Classify the preparation.
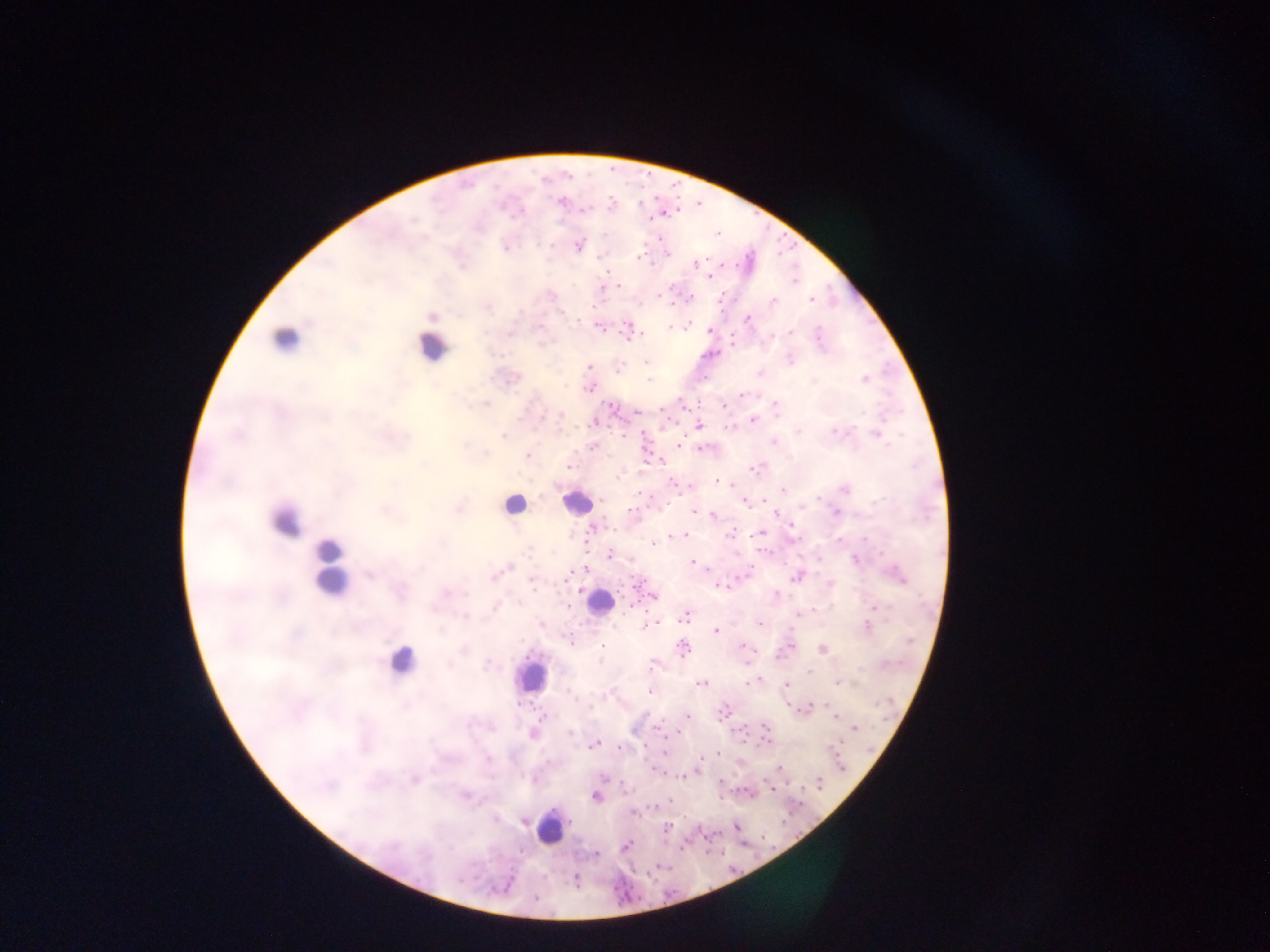

Thick blood film.

{
  "capture": "mobile-phone photograph through a microscope",
  "country": "Ghana",
  "leukocyte_locations": "approximate centers as (x, y) in pixels: (287, 337), (432, 346), (577, 502), (514, 505), (285, 520), (330, 566), (599, 603), (400, 660), (530, 674), (549, 828)",
  "image_size": "1270×952 pixels",
  "field_of_view": "single",
  "plasmodium_parasite_locations": "approximate centers as (x, y) in pixels: (559, 200), (611, 204), (584, 210), (716, 233), (577, 245), (505, 246), (639, 256), (694, 263), (710, 276), (795, 281), (617, 285), (671, 287), (690, 298), (812, 299), (671, 302), (771, 302), (432, 315), (747, 319), (599, 325), (686, 326), (711, 330), (791, 331), (628, 332), (731, 343), (711, 353), (646, 362), (590, 367), (617, 368), (864, 379), (589, 387), (742, 393), (775, 404), (611, 406), (683, 406), (725, 406), (637, 411), (560, 416), (752, 420), (594, 423), (699, 425), (877, 433), (503, 436), (592, 446), (679, 446), (701, 447), (526, 455), (661, 461), (568, 467), (756, 468), (718, 481), (844, 488), (783, 489), (744, 501), (773, 511), (836, 511), (631, 512), (695, 512), (713, 515), (791, 528), (593, 529), (728, 532), (759, 533), (685, 535), (654, 544), (608, 555), (818, 558), (693, 561), (508, 567), (585, 570), (747, 571), (796, 576), (897, 576), (830, 584), (719, 585), (653, 597), (630, 605), (873, 606), (567, 607), (796, 613), (684, 617), (649, 623), (758, 623), (867, 627), (715, 630), (741, 645), (602, 646), (789, 646), (682, 649), (822, 649), (746, 661), (651, 666), (807, 671), (756, 680), (753, 682), (837, 682), (699, 683), (786, 685), (649, 691), (807, 708), (723, 711), (686, 716), (541, 717), (836, 717), (656, 727), (854, 728), (765, 729), (533, 733), (678, 733), (764, 741), (594, 745), (618, 748), (664, 752), (717, 753), (780, 767), (697, 770), (413, 780), (820, 783), (772, 788), (747, 792), (596, 796), (633, 812), (736, 825), (666, 827), (625, 846), (595, 853), (575, 879), (535, 898)"
}